Assess this cell for malaria.
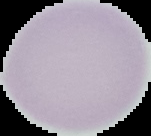

It is uninfected.

From a thin blood smear. Segmented cell region on a black background. Image is 151×136 pixels.